Report the malaria status of this cell.
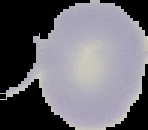
Uninfected.

Image is 148×130 pixels. From a thin blood smear. Cell region segmented out of the field of view; the surrounding area is masked to black.